Assess the morphology of the erythrocytes.
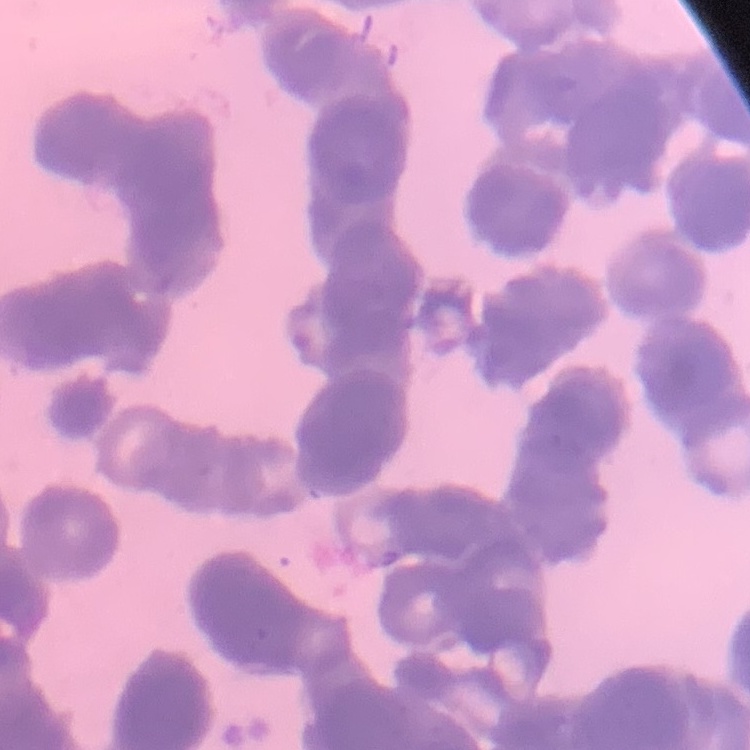

They show rouleaux formation.

Thin blood smear. Square crop of a larger photomicrograph. Stained with either Field's or Giemsa.